Describe the morphology of the erythrocytes.
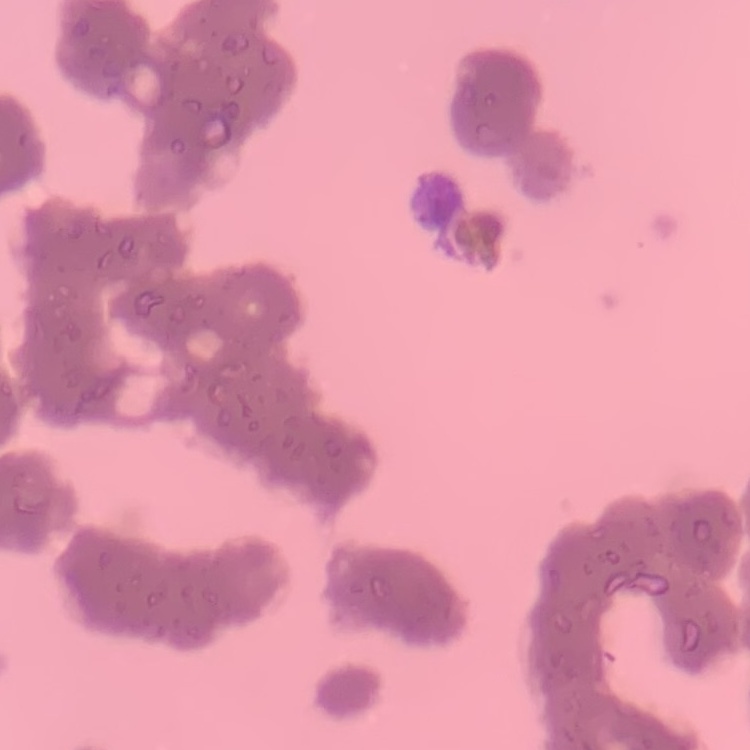
They show rouleaux formation.

Thin peripheral smear. Square crop of a larger photomicrograph. Field's or Giemsa stain.